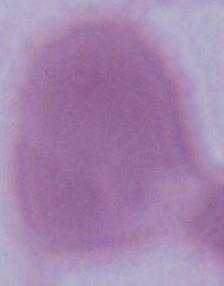

magnification = 1000x
modality = micrograph
identification = red blood cell